Report the malaria status of this cell.
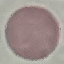
It is uninfected.

capture = smartphone through the microscope eyepiece
preparation = thin smear
stain = Giemsa
image type = automatically extracted cell patch, resized to 64 × 64 pixels